Describe the morphology of the red blood cells.
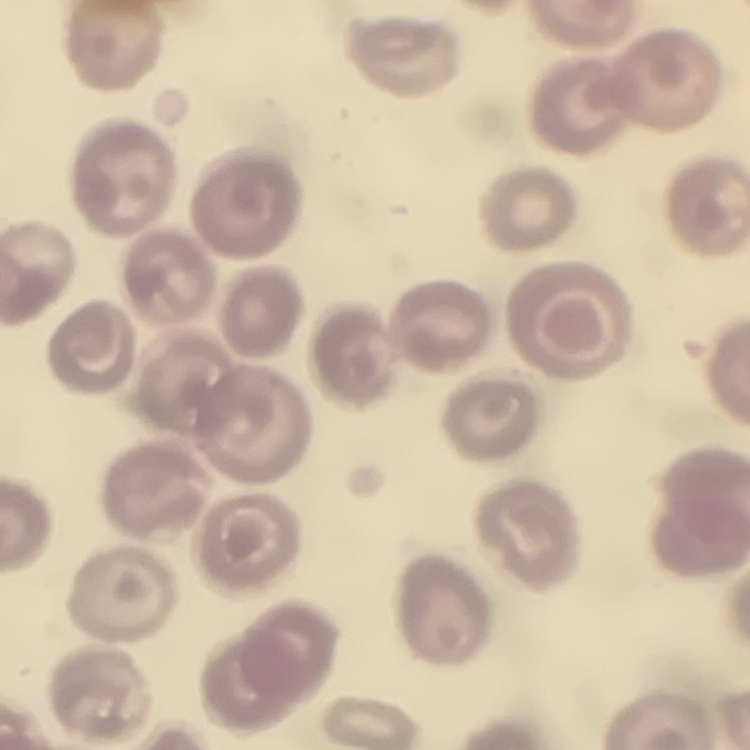
No rouleaux formation.

Summary:
  - Image type: one tile cut from a larger photomicrograph
  - Stain: Field's or Giemsa
  - Preparation: thin blood smear